Locate and identify every blood parasite.
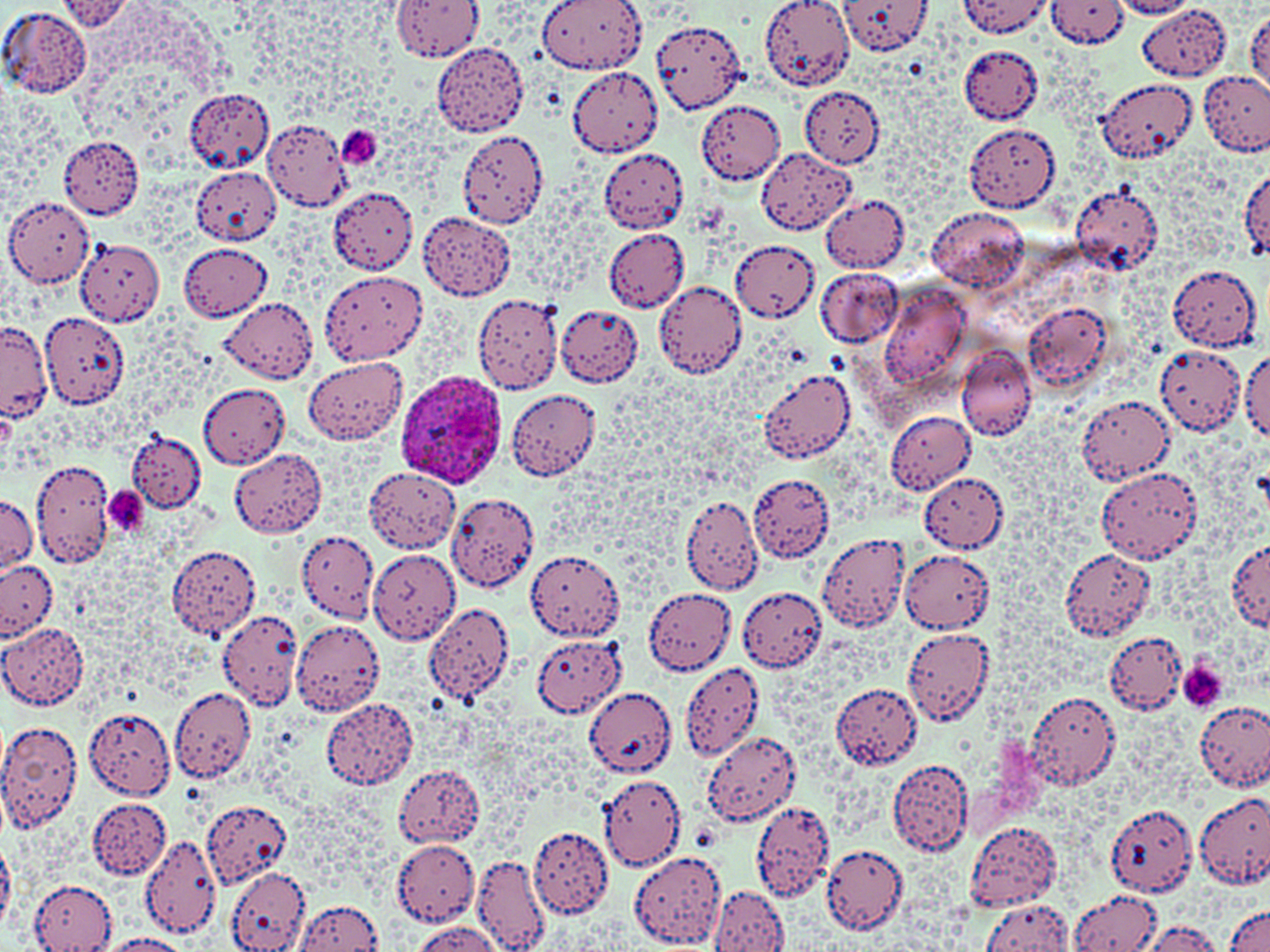

Approximate bounding boxes as [x1, y1, x2, y2] in pixels.
Plasmodium ovale-infected red blood cells: [399, 371, 507, 490].
No Plasmodium falciparum, Plasmodium malariae, Plasmodium vivax, Babesia divergens, or Trypanosoma brucei observed.

slide-level diagnosis = Plasmodium ovale
image size = 1270×952 pixels
field of view = single
magnification = 1000x
modality = light microscopy
preparation = thin blood smear
uninfected red blood cell locations = approximate bounding boxes as [x1, y1, x2, y2] in pixels: [539, 0, 647, 73], [759, 0, 850, 91], [836, 0, 933, 56], [958, 0, 1052, 36], [391, 1, 484, 63], [1047, 1, 1131, 48], [1110, 1, 1199, 18], [58, 2, 135, 33], [0, 5, 91, 99], [1137, 5, 1231, 82], [1246, 12, 1270, 94], [650, 18, 748, 114], [432, 42, 530, 137], [959, 45, 1042, 124], [565, 67, 664, 158], [1198, 70, 1270, 157], [1100, 78, 1199, 164], [183, 87, 275, 171], [800, 87, 885, 167], [698, 99, 785, 185], [261, 120, 352, 209], [337, 121, 383, 171], [963, 122, 1061, 212], [457, 131, 546, 232], [59, 137, 144, 220], [756, 147, 856, 233], [598, 148, 690, 232], [191, 167, 281, 245], [1238, 169, 1269, 261], [1070, 182, 1164, 276], [328, 186, 418, 273], [820, 193, 910, 272], [3, 198, 93, 289], [927, 207, 1028, 292], [418, 212, 515, 298], [600, 229, 689, 311], [75, 238, 164, 327], [729, 239, 819, 322], [179, 244, 271, 320], [1168, 264, 1262, 351], [816, 267, 903, 348], [318, 270, 428, 364], [654, 279, 749, 379], [881, 284, 970, 386], [472, 292, 564, 395], [220, 299, 320, 384], [1023, 302, 1117, 391], [556, 305, 642, 386], [41, 310, 130, 410], [0, 323, 53, 421], [1152, 343, 1247, 436], [955, 344, 1037, 439], [1241, 351, 1270, 443], [302, 357, 407, 445], [757, 368, 858, 464], [197, 382, 289, 469], [507, 389, 602, 480], [1075, 394, 1175, 485], [884, 410, 976, 495], [127, 433, 206, 512], [230, 449, 327, 538], [33, 459, 117, 567], [1096, 466, 1203, 564], [363, 468, 461, 553], [748, 472, 834, 563], [919, 473, 1008, 551], [448, 493, 540, 592], [679, 494, 764, 594], [1, 496, 38, 576], [817, 529, 912, 635], [297, 530, 378, 622], [1225, 539, 1267, 632], [167, 545, 261, 639], [1060, 548, 1154, 641], [369, 549, 461, 645], [525, 549, 626, 641], [900, 550, 994, 632], [0, 560, 56, 639], [736, 588, 828, 671], [642, 589, 735, 675], [423, 601, 516, 706], [217, 610, 304, 710], [290, 620, 384, 715], [0, 624, 89, 710], [902, 627, 995, 726], [1102, 630, 1189, 716], [529, 632, 627, 719], [679, 660, 764, 761], [831, 683, 924, 769], [169, 686, 256, 782], [584, 688, 674, 775], [1026, 690, 1120, 791], [322, 695, 418, 790], [1195, 699, 1270, 793], [84, 707, 179, 800], [0, 719, 84, 831], [703, 732, 795, 827], [887, 759, 974, 857], [391, 763, 483, 848], [598, 773, 686, 870], [1196, 791, 1270, 889], [88, 798, 171, 880], [200, 799, 292, 890], [752, 800, 832, 898], [1105, 803, 1199, 896], [965, 821, 1061, 910], [529, 827, 614, 918], [140, 834, 220, 940], [390, 837, 480, 926], [0, 838, 18, 933], [822, 844, 908, 934], [628, 849, 726, 948], [472, 852, 551, 950], [225, 866, 310, 952], [29, 877, 116, 950], [708, 887, 789, 952], [1071, 888, 1165, 952], [293, 899, 385, 950], [979, 899, 1075, 951], [1225, 906, 1269, 952], [1138, 920, 1228, 952], [408, 921, 502, 951], [100, 934, 191, 952]
platelet locations = approximate bounding boxes as [x1, y1, x2, y2] in pixels: [338, 125, 384, 170], [103, 486, 149, 534], [1176, 662, 1229, 712]
stain = May-Grünwald-Giemsa